Comment on the morphology of the erythrocytes.
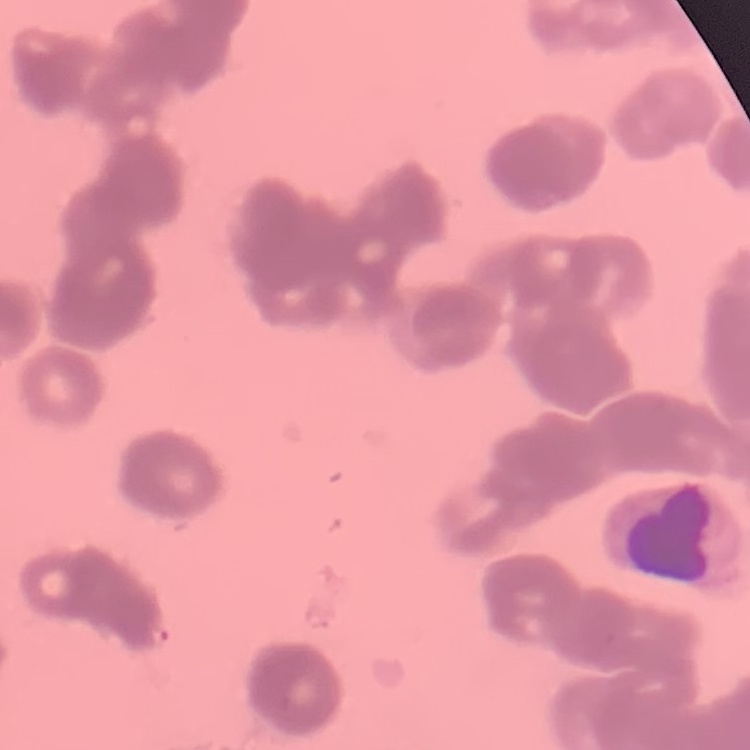
Rouleaux formation.

Summary:
  - Preparation: thin blood film
  - Stain: Field's or Giemsa
  - Image type: square crop of a larger photomicrograph